Assess this cell for malaria.
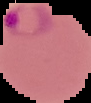

It is parasitized.

image_type: cell region segmented out of the field of view; surrounding area masked to black
preparation: thin blood smear
image_size: 91×103 pixels